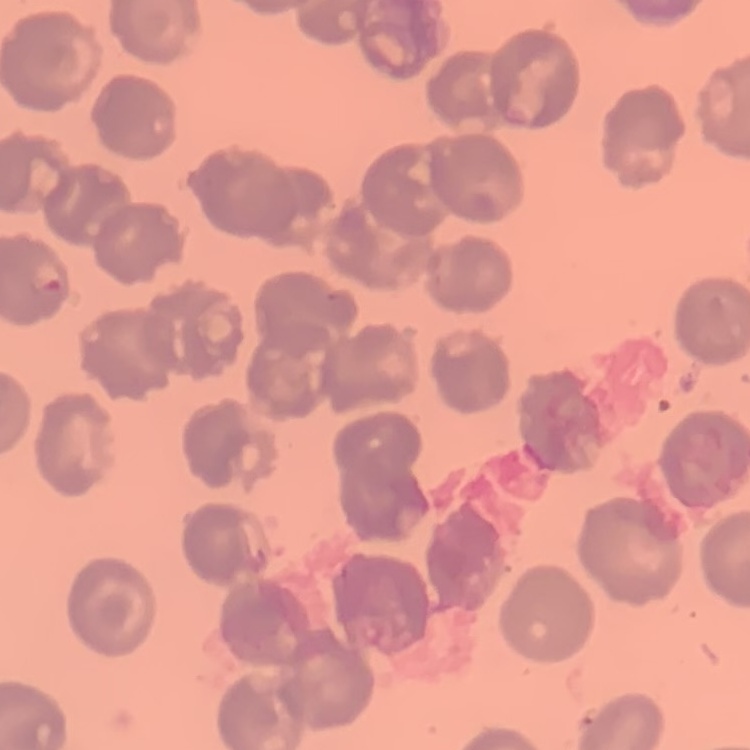
Summary:
  - Red blood cell morphology: no rouleaux formation
  - Stain: Field's or Giemsa
  - Preparation: thin peripheral smear
  - Image type: square crop of a larger photomicrograph